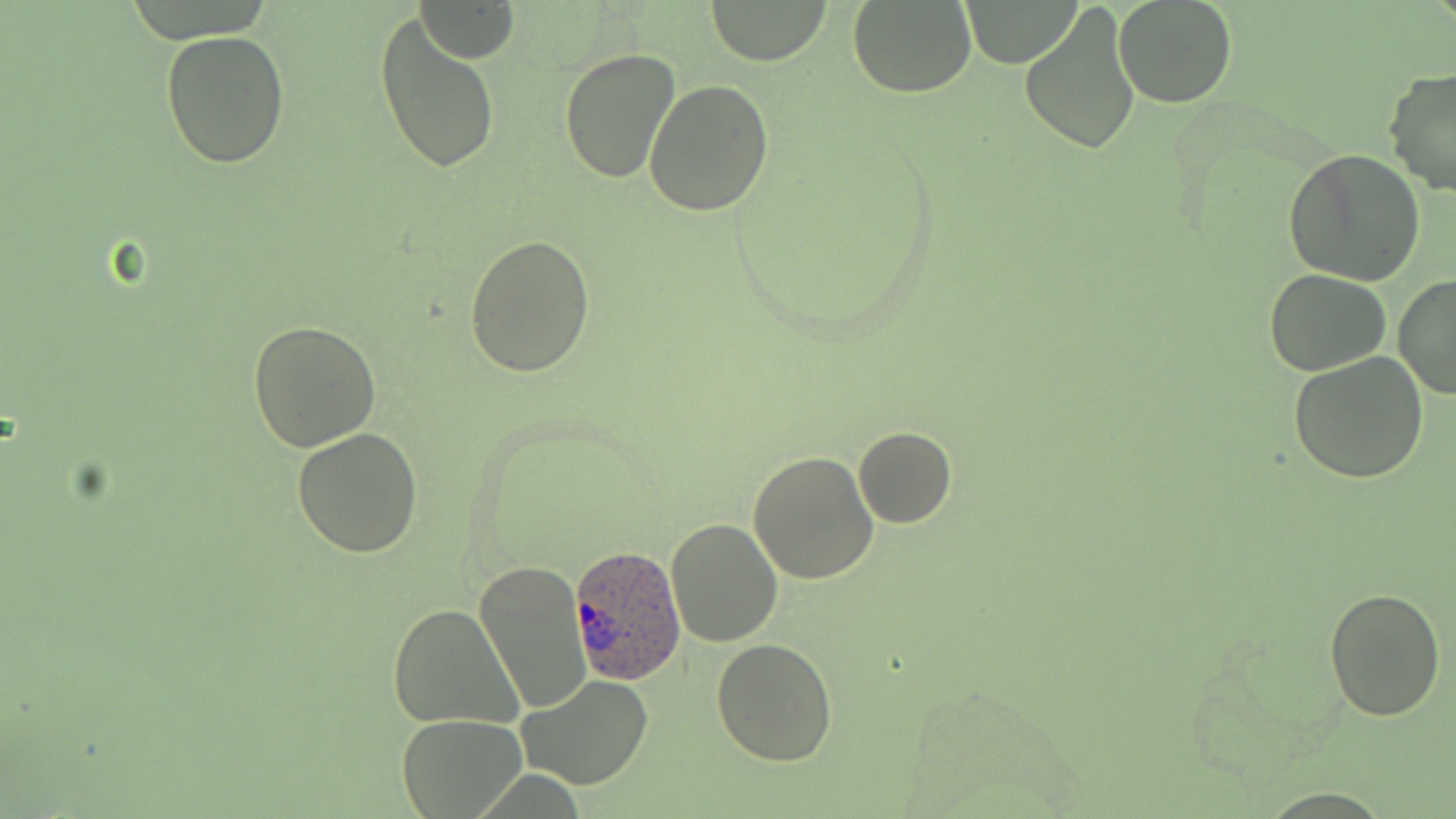

Summary:
  - Coordinate format: approximate bounding boxes as named x1/y1/x2/y2 corners in pixels
  - Plasmodium ovale-infected red blood cell locations: (x1=570, y1=544, x2=687, y2=687)
  - Uninfected red blood cell locations: (x1=702, y1=0, x2=836, y2=65), (x1=848, y1=1, x2=977, y2=98), (x1=957, y1=1, x2=1083, y2=65), (x1=1113, y1=1, x2=1238, y2=110), (x1=416, y1=2, x2=520, y2=63), (x1=1018, y1=3, x2=1141, y2=157), (x1=372, y1=12, x2=502, y2=178), (x1=161, y1=29, x2=290, y2=169), (x1=557, y1=47, x2=681, y2=183), (x1=1382, y1=66, x2=1456, y2=196), (x1=644, y1=79, x2=774, y2=216), (x1=1285, y1=147, x2=1426, y2=286), (x1=465, y1=234, x2=597, y2=377), (x1=1265, y1=268, x2=1390, y2=377), (x1=1392, y1=274, x2=1456, y2=401), (x1=249, y1=318, x2=381, y2=452), (x1=1288, y1=352, x2=1428, y2=484), (x1=852, y1=426, x2=957, y2=529), (x1=291, y1=428, x2=424, y2=558), (x1=748, y1=449, x2=879, y2=586), (x1=664, y1=516, x2=782, y2=648), (x1=474, y1=560, x2=590, y2=712), (x1=1323, y1=586, x2=1447, y2=722), (x1=387, y1=603, x2=522, y2=731), (x1=711, y1=638, x2=838, y2=767), (x1=516, y1=674, x2=655, y2=790), (x1=397, y1=713, x2=528, y2=817)
  - Slide-level diagnosis: Plasmodium ovale
  - Magnification: 1000x
  - Image size: 1456×819 pixels
  - Modality: light microscopy
  - Stain: May-Grünwald-Giemsa
  - Preparation: thin blood smear
  - Field of view: one of a larger specimen